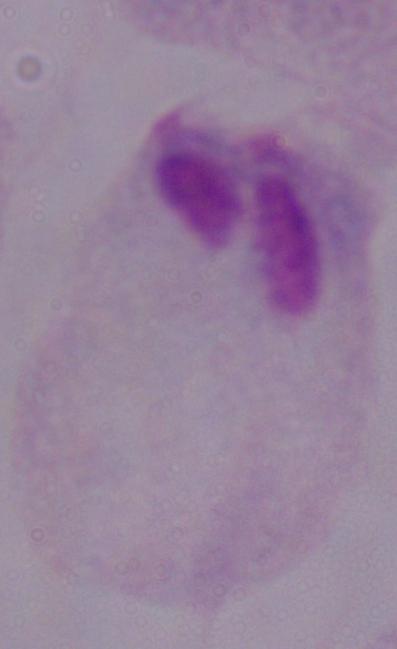
A trichomonad is seen. Captured at 1000x magnification. Micrograph.